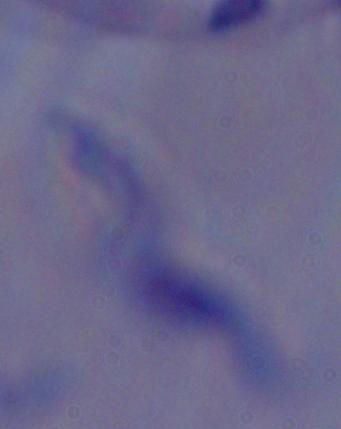

Summary:
  - Identification: trypanosome
  - Modality: micrograph
  - Magnification: 1000x